Give the position of every leukocyte visible.
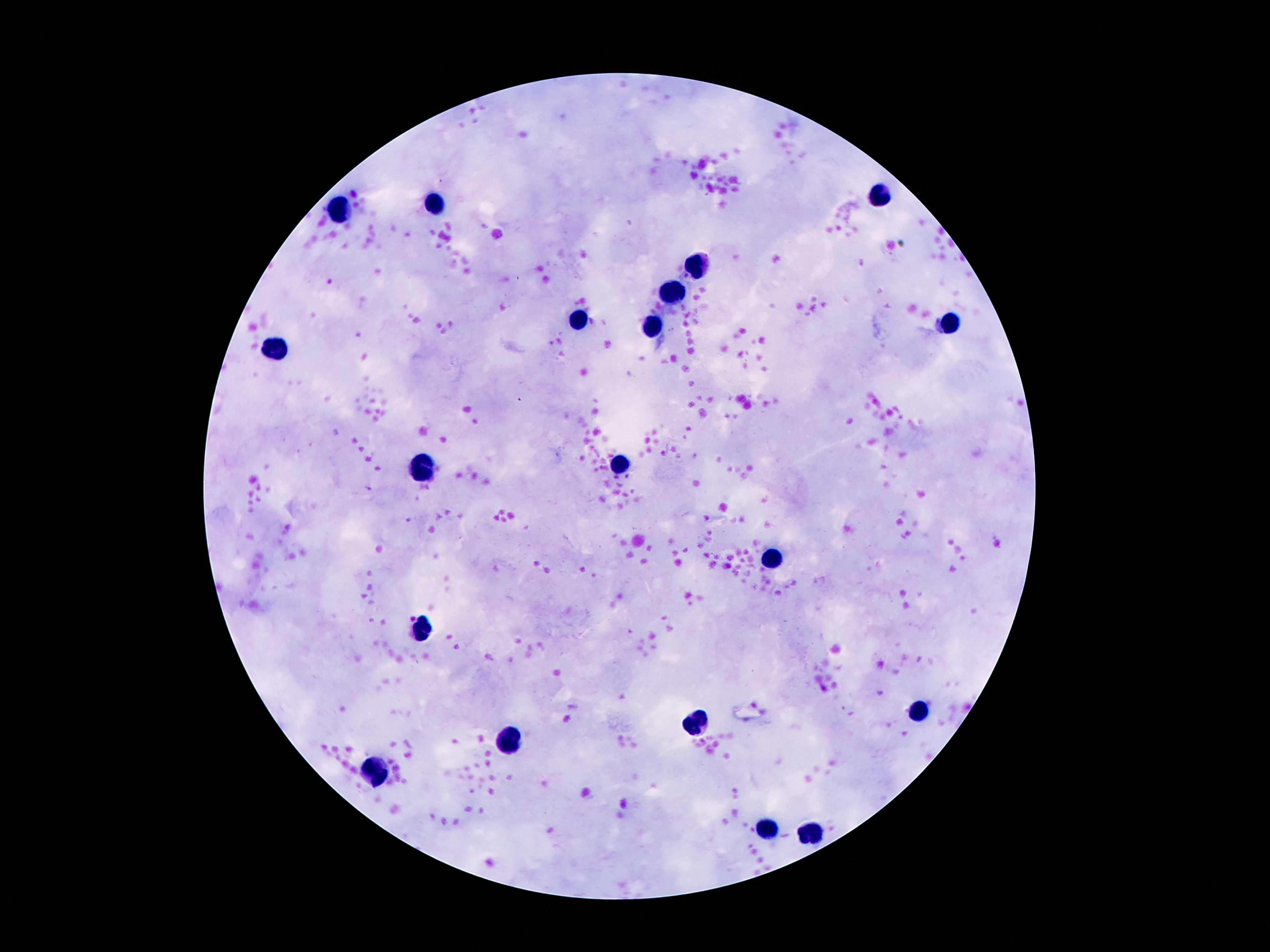
Approximate object centers, in pixels from the top-left corner.
Leukocytes: (x=879, y=196), (x=435, y=204), (x=340, y=210), (x=702, y=265), (x=673, y=291), (x=582, y=320), (x=949, y=322), (x=652, y=329), (x=274, y=346), (x=421, y=465), (x=618, y=465), (x=771, y=560), (x=421, y=627), (x=918, y=712), (x=697, y=725), (x=508, y=737), (x=375, y=770), (x=771, y=828), (x=813, y=830).

image size = 1270×952 pixels
capture = smartphone camera through the microscope eyepiece
stain = Giemsa
preparation = thick blood film
patient malaria status = negative
field of view = single
magnification = 100x